Assess the morphology of the erythrocytes.
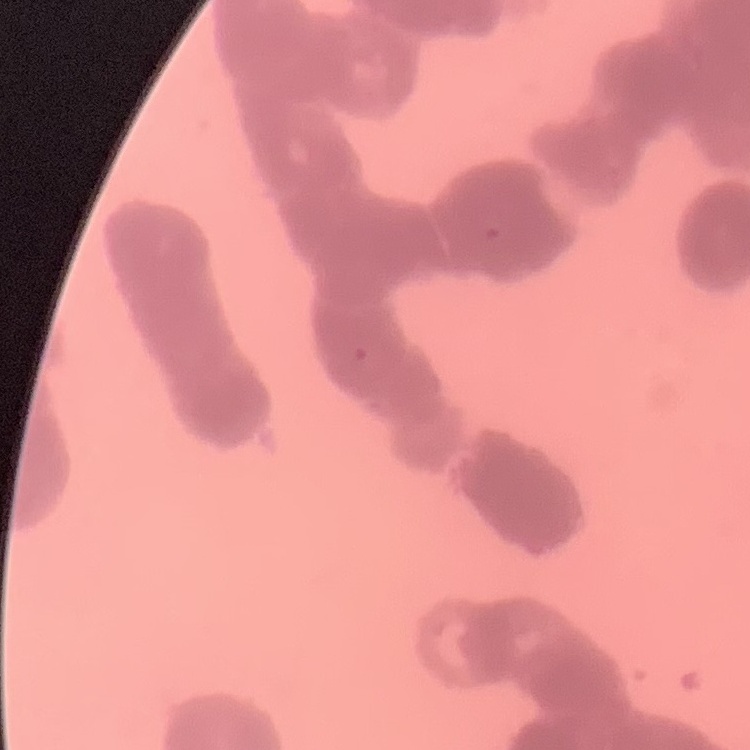
They show rouleaux formation.

Summary:
  - Image type: square crop of a larger photomicrograph
  - Stain: Field's or Giemsa
  - Preparation: thin peripheral smear